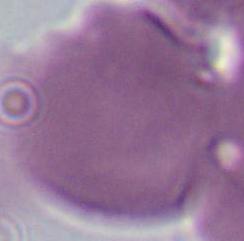
Micrograph. 1000x magnification. An erythrocyte is seen.